Locate and identify every blood parasite.
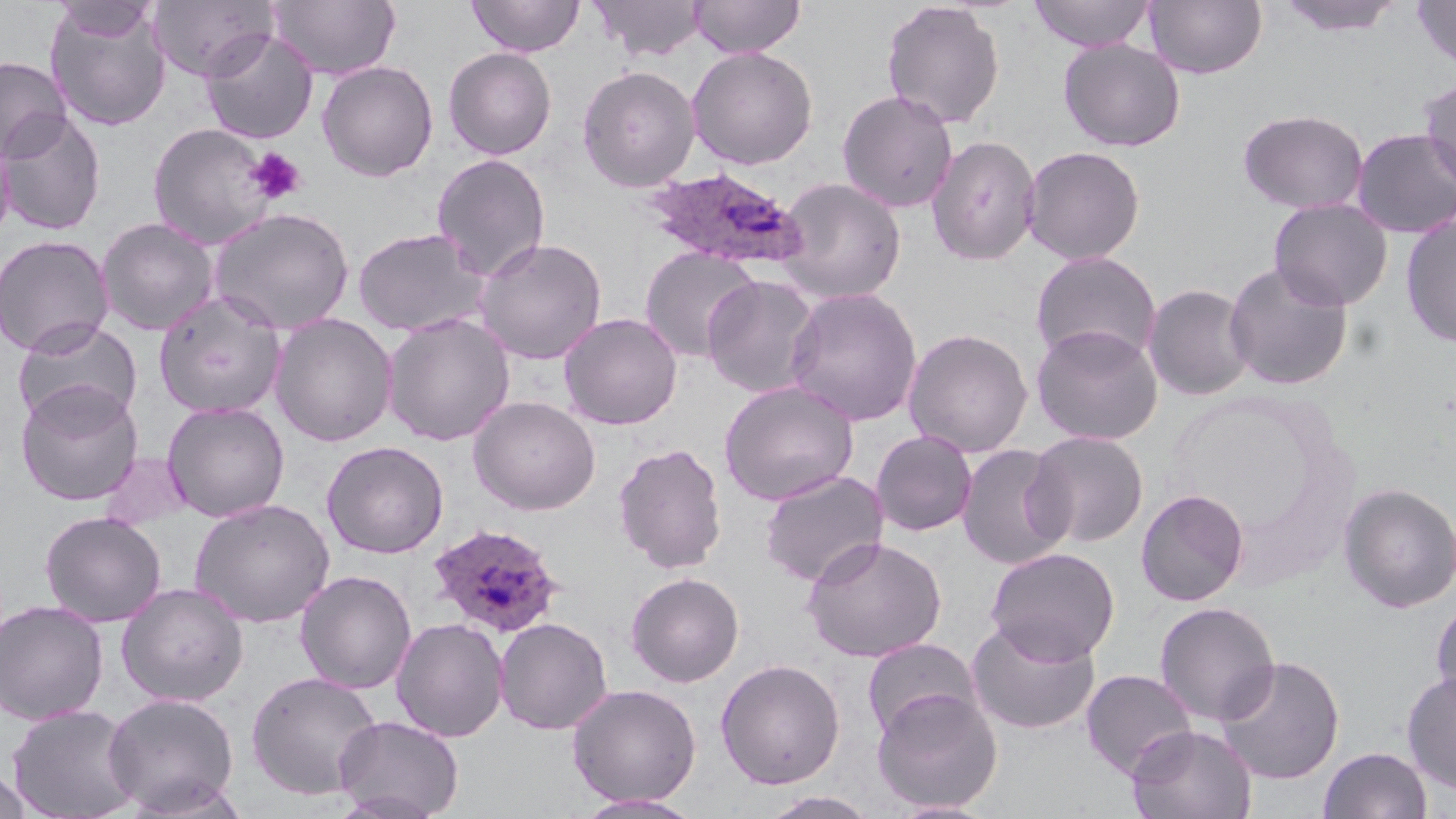

Approximate bounding boxes as named x1/y1/x2/y2 corners in pixels.
Plasmodium ovale-infected red blood cells: (x1=638, y1=167, x2=808, y2=272), (x1=426, y1=522, x2=566, y2=639).
No Plasmodium falciparum, Plasmodium malariae, Plasmodium vivax, Babesia divergens, or Trypanosoma brucei observed.

Summary:
  - Uninfected red blood cell locations: (x1=51, y1=0, x2=160, y2=41), (x1=268, y1=0, x2=401, y2=79), (x1=467, y1=0, x2=585, y2=57), (x1=591, y1=0, x2=707, y2=60), (x1=689, y1=0, x2=805, y2=58), (x1=1028, y1=0, x2=1156, y2=52), (x1=1144, y1=0, x2=1268, y2=79), (x1=1274, y1=0, x2=1406, y2=37), (x1=148, y1=1, x2=277, y2=82), (x1=881, y1=1, x2=1005, y2=129), (x1=1412, y1=1, x2=1456, y2=73), (x1=46, y1=6, x2=171, y2=130), (x1=200, y1=29, x2=318, y2=144), (x1=1058, y1=39, x2=1186, y2=152), (x1=687, y1=46, x2=818, y2=169), (x1=443, y1=47, x2=556, y2=160), (x1=0, y1=56, x2=71, y2=161), (x1=317, y1=61, x2=438, y2=182), (x1=577, y1=64, x2=700, y2=192), (x1=1418, y1=76, x2=1456, y2=193), (x1=836, y1=89, x2=959, y2=213), (x1=1237, y1=108, x2=1370, y2=214), (x1=1, y1=111, x2=106, y2=236), (x1=147, y1=122, x2=278, y2=250), (x1=1351, y1=127, x2=1456, y2=238), (x1=0, y1=129, x2=15, y2=248), (x1=925, y1=134, x2=1042, y2=266), (x1=1021, y1=145, x2=1146, y2=264), (x1=431, y1=154, x2=551, y2=282), (x1=774, y1=177, x2=907, y2=303), (x1=1268, y1=198, x2=1393, y2=311), (x1=208, y1=206, x2=355, y2=335), (x1=1400, y1=212, x2=1456, y2=348), (x1=96, y1=217, x2=220, y2=336), (x1=352, y1=227, x2=488, y2=337), (x1=0, y1=235, x2=114, y2=356), (x1=474, y1=237, x2=607, y2=364), (x1=640, y1=246, x2=760, y2=362), (x1=1029, y1=251, x2=1162, y2=367), (x1=1223, y1=261, x2=1354, y2=391), (x1=701, y1=274, x2=823, y2=398), (x1=1143, y1=283, x2=1256, y2=401), (x1=785, y1=287, x2=923, y2=426), (x1=153, y1=292, x2=287, y2=418), (x1=559, y1=312, x2=682, y2=430), (x1=270, y1=313, x2=398, y2=447), (x1=382, y1=313, x2=515, y2=446), (x1=12, y1=316, x2=143, y2=431), (x1=1031, y1=324, x2=1164, y2=445), (x1=902, y1=327, x2=1033, y2=458), (x1=718, y1=380, x2=859, y2=506), (x1=15, y1=382, x2=144, y2=506), (x1=468, y1=396, x2=601, y2=515), (x1=162, y1=401, x2=290, y2=522), (x1=870, y1=429, x2=977, y2=536), (x1=1025, y1=429, x2=1150, y2=548), (x1=321, y1=440, x2=448, y2=558), (x1=613, y1=442, x2=728, y2=574), (x1=956, y1=443, x2=1072, y2=570), (x1=99, y1=452, x2=193, y2=530), (x1=759, y1=470, x2=889, y2=587), (x1=1337, y1=482, x2=1456, y2=614), (x1=1135, y1=488, x2=1249, y2=607), (x1=189, y1=498, x2=335, y2=628), (x1=39, y1=511, x2=166, y2=627), (x1=802, y1=535, x2=947, y2=662), (x1=985, y1=546, x2=1120, y2=664), (x1=295, y1=570, x2=417, y2=694), (x1=625, y1=572, x2=745, y2=687), (x1=116, y1=582, x2=249, y2=706), (x1=1429, y1=597, x2=1456, y2=713), (x1=0, y1=600, x2=109, y2=724), (x1=1153, y1=601, x2=1280, y2=726), (x1=391, y1=617, x2=509, y2=742), (x1=494, y1=617, x2=613, y2=735), (x1=966, y1=618, x2=1101, y2=736), (x1=861, y1=638, x2=982, y2=741), (x1=1214, y1=655, x2=1346, y2=784), (x1=714, y1=658, x2=845, y2=789), (x1=1080, y1=668, x2=1198, y2=780), (x1=1401, y1=669, x2=1456, y2=794), (x1=245, y1=670, x2=384, y2=801), (x1=566, y1=683, x2=702, y2=806), (x1=871, y1=688, x2=1003, y2=813), (x1=103, y1=692, x2=240, y2=815), (x1=6, y1=705, x2=143, y2=819), (x1=333, y1=715, x2=464, y2=819), (x1=1127, y1=724, x2=1257, y2=819), (x1=1317, y1=746, x2=1433, y2=819), (x1=0, y1=767, x2=32, y2=819), (x1=759, y1=791, x2=881, y2=819), (x1=573, y1=793, x2=707, y2=818), (x1=886, y1=799, x2=999, y2=818)
  - Platelet locations: (x1=245, y1=146, x2=307, y2=204)
  - Slide-level diagnosis: Plasmodium ovale
  - Stain: May-Grünwald-Giemsa
  - Preparation: thin blood smear
  - Field of view: one of a larger specimen
  - Modality: light microscopy
  - Image size: 1456×819 pixels
  - Magnification: 1000x